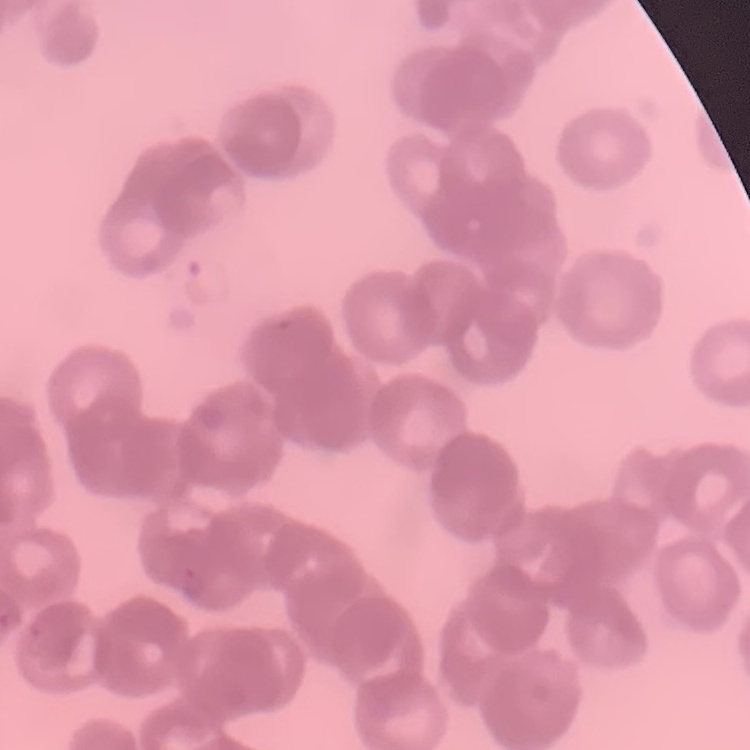

red blood cell morphology = rouleaux formation
stain = Field's or Giemsa
image type = one tile cut from a larger photomicrograph
preparation = thin blood smear